Give the extent of all Plasmodium malariae-infected red blood cells.
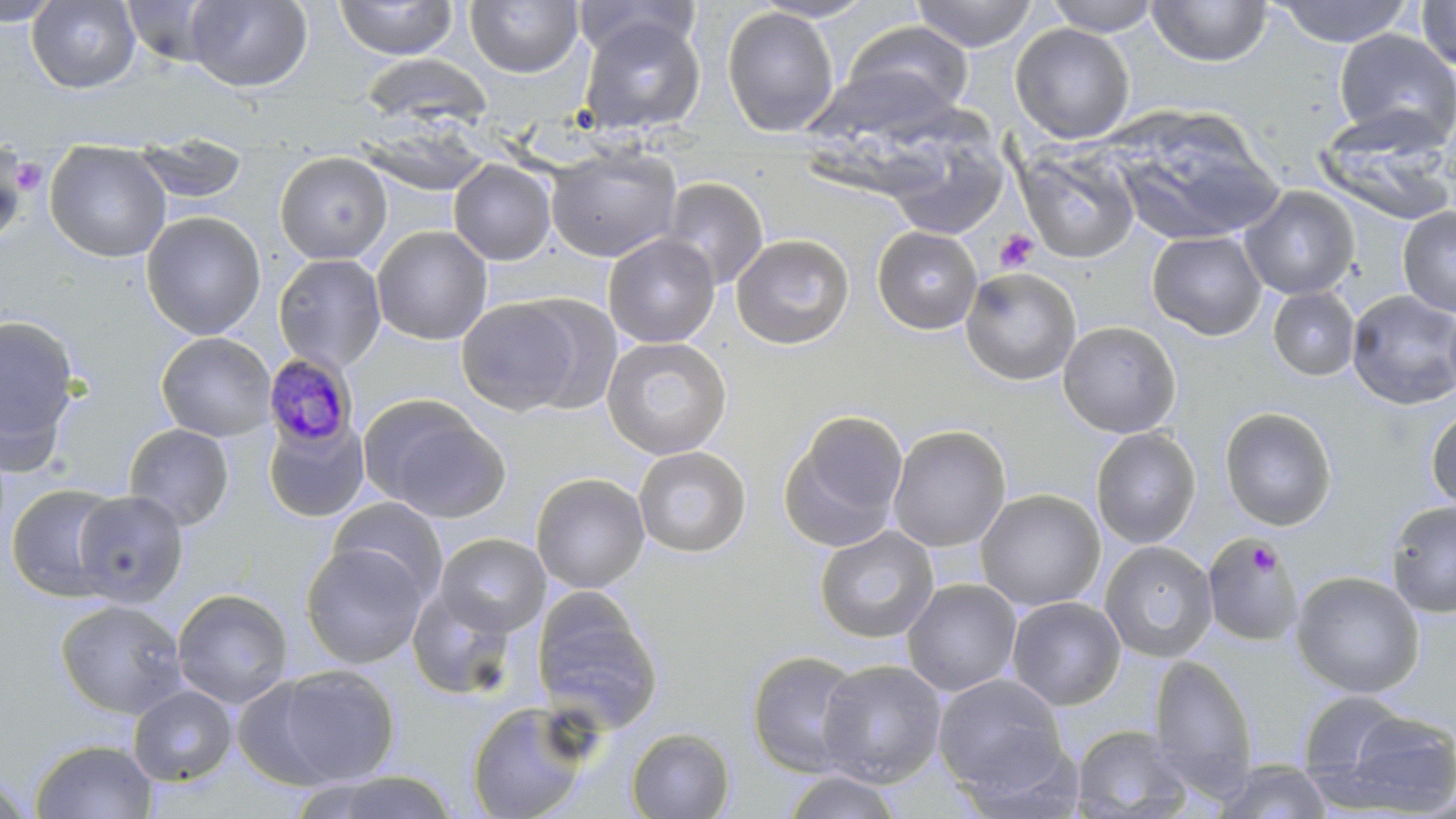

Approximate bounding boxes as [x1, y1, x2, y2] in pixels.
Plasmodium malariae-infected red blood cells: [263, 352, 359, 449].

Summary:
  - Uninfected red blood cell locations: [0, 0, 63, 27], [26, 0, 141, 93], [185, 0, 311, 92], [571, 0, 700, 61], [750, 0, 877, 23], [910, 0, 1040, 51], [1042, 0, 1163, 36], [1146, 0, 1272, 67], [1272, 0, 1415, 47], [121, 1, 229, 68], [333, 1, 458, 60], [465, 1, 583, 77], [1416, 1, 1456, 72], [721, 6, 840, 138], [578, 14, 706, 137], [837, 21, 976, 123], [1010, 23, 1135, 143], [1333, 29, 1456, 147], [360, 54, 489, 128], [807, 63, 963, 148], [1110, 111, 1281, 246], [1316, 114, 1456, 228], [361, 117, 489, 197], [887, 132, 1009, 240], [131, 133, 249, 205], [44, 140, 172, 262], [1, 144, 31, 250], [1014, 144, 1141, 264], [545, 145, 682, 262], [274, 151, 392, 264], [448, 159, 557, 265], [662, 177, 769, 290], [1240, 186, 1360, 300], [637, 202, 756, 325], [1397, 205, 1456, 315], [140, 210, 266, 340], [371, 225, 493, 345], [872, 226, 982, 334], [1147, 231, 1267, 341], [603, 233, 720, 348], [731, 233, 855, 350], [273, 253, 387, 372], [960, 266, 1082, 386], [1268, 287, 1360, 381], [1347, 290, 1456, 410], [511, 294, 623, 415], [456, 298, 580, 416], [1442, 299, 1456, 405], [0, 312, 82, 470], [1058, 320, 1181, 439], [156, 331, 277, 442], [601, 336, 732, 460], [367, 401, 509, 521], [1219, 406, 1337, 531], [1425, 406, 1456, 512], [779, 409, 909, 553], [263, 415, 370, 523], [124, 423, 234, 530], [886, 424, 1011, 552], [1090, 427, 1201, 549], [632, 445, 752, 557], [530, 473, 650, 593], [6, 482, 125, 602], [974, 489, 1106, 611], [72, 490, 189, 608], [327, 496, 448, 603], [1385, 500, 1456, 618], [814, 526, 939, 644], [434, 532, 550, 637], [1202, 534, 1302, 649], [1099, 540, 1217, 663], [301, 543, 428, 669], [1290, 571, 1425, 699], [902, 578, 1022, 697], [407, 587, 519, 701], [172, 588, 293, 708], [532, 592, 664, 734], [1006, 596, 1126, 710], [55, 599, 189, 720], [746, 650, 867, 778], [1148, 654, 1258, 800], [816, 659, 947, 787], [273, 664, 400, 785], [933, 673, 1067, 794], [232, 676, 346, 790], [128, 685, 238, 786], [1296, 690, 1410, 786], [466, 699, 598, 819], [1335, 711, 1456, 815], [1070, 724, 1194, 819], [626, 728, 736, 818], [30, 739, 158, 819], [1215, 759, 1333, 819], [779, 769, 903, 818], [308, 770, 462, 818], [1, 771, 37, 817]
  - Platelet locations: [8, 159, 47, 197], [995, 229, 1039, 274], [1248, 542, 1281, 578]
  - Slide-level diagnosis: Plasmodium malariae
  - Field of view: single
  - Modality: light microscopy
  - Stain: May-Grünwald-Giemsa
  - Magnification: 1000x
  - Preparation: thin blood smear
  - Image size: 1456×819 pixels